State which cell type is depicted.
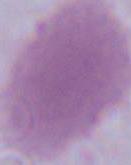

An erythrocyte.

Captured at 1000x magnification. Micrograph.